Locate every leukocyte (white blood cell).
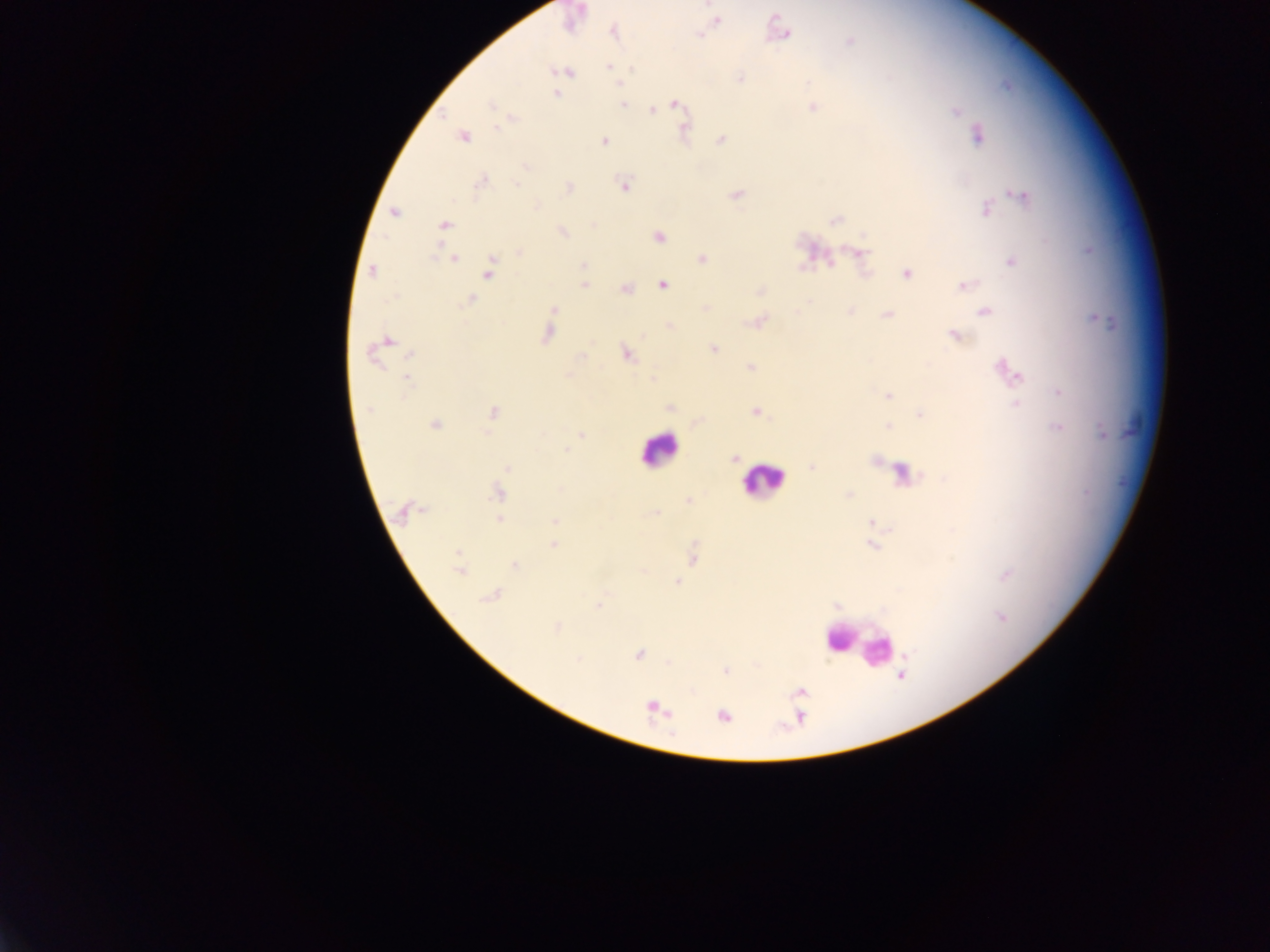
Approximate centers as {x, y} in pixels.
Leukocytes: {659, 450}, {763, 479}, {838, 636}, {863, 644}, {879, 653}.

Plasmodium parasite locations: {715, 19}, {613, 31}, {699, 34}, {783, 34}, {850, 41}, {608, 66}, {563, 71}, {740, 78}, {618, 83}, {556, 93}, {621, 104}, {675, 104}, {812, 106}, {652, 108}, {956, 111}, {511, 118}, {684, 131}, {978, 135}, {462, 136}, {720, 139}, {604, 140}, {482, 181}, {624, 184}, {567, 187}, {736, 193}, {1020, 194}, {986, 209}, {394, 212}, {835, 219}, {444, 225}, {562, 231}, {658, 236}, {519, 251}, {857, 252}, {453, 258}, {702, 258}, {1011, 260}, {583, 265}, {489, 270}, {372, 271}, {906, 273}, {662, 283}, {583, 284}, {962, 285}, {625, 288}, {761, 291}, {469, 299}, {705, 309}, {553, 310}, {984, 310}, {849, 311}, {887, 313}, {758, 320}, {669, 327}, {547, 332}, {953, 335}, {385, 341}, {713, 348}, {376, 350}, {626, 353}, {750, 367}, {1006, 371}, {566, 375}, {407, 377}, {653, 378}, {1059, 392}, {887, 394}, {1016, 405}, {669, 407}, {756, 411}, {492, 412}, {920, 414}, {697, 421}, {434, 424}, {888, 425}, {1058, 427}, {1102, 432}, {581, 435}, {734, 458}, {507, 467}, {812, 467}, {498, 492}, {848, 494}, {688, 501}, {406, 510}, {653, 514}, {499, 519}, {555, 521}, {553, 544}, {870, 544}, {692, 555}, {460, 564}, {515, 564}, {1006, 575}, {676, 582}, {491, 595}, {599, 605}, {836, 606}, {556, 627}, {639, 654}, {669, 662}, {726, 670}, {800, 693}, {653, 707}, {723, 716}. Thick blood film. Collected in Ghana. Single field of view. Image is 1270×952 pixels. Photographed through a microscope with a mobile-phone camera.